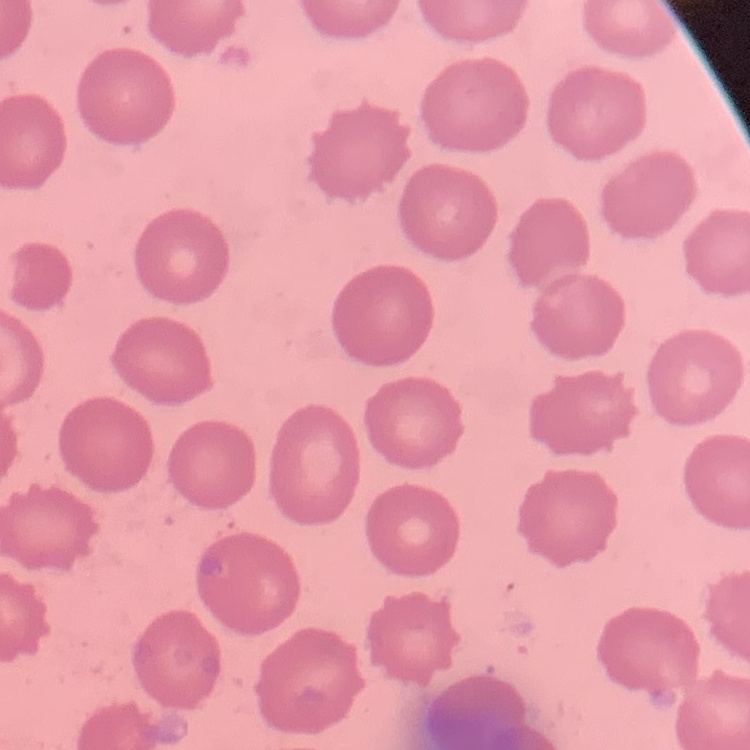
Summary:
  - Erythrocyte morphology: no rouleaux formation
  - Image type: one tile cut from a larger photomicrograph
  - Preparation: thin blood smear
  - Stain: Field's or Giemsa